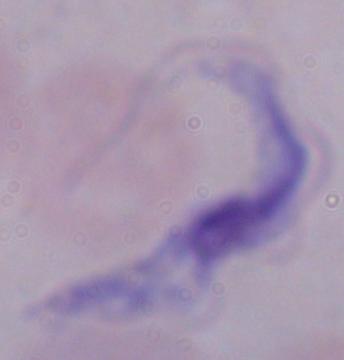

A trypanosome is shown. 1000x magnification. Micrograph.